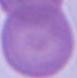 A red blood cell is seen. 1000x magnification. Photomicrograph.